Locate every uninfected red blood cell.
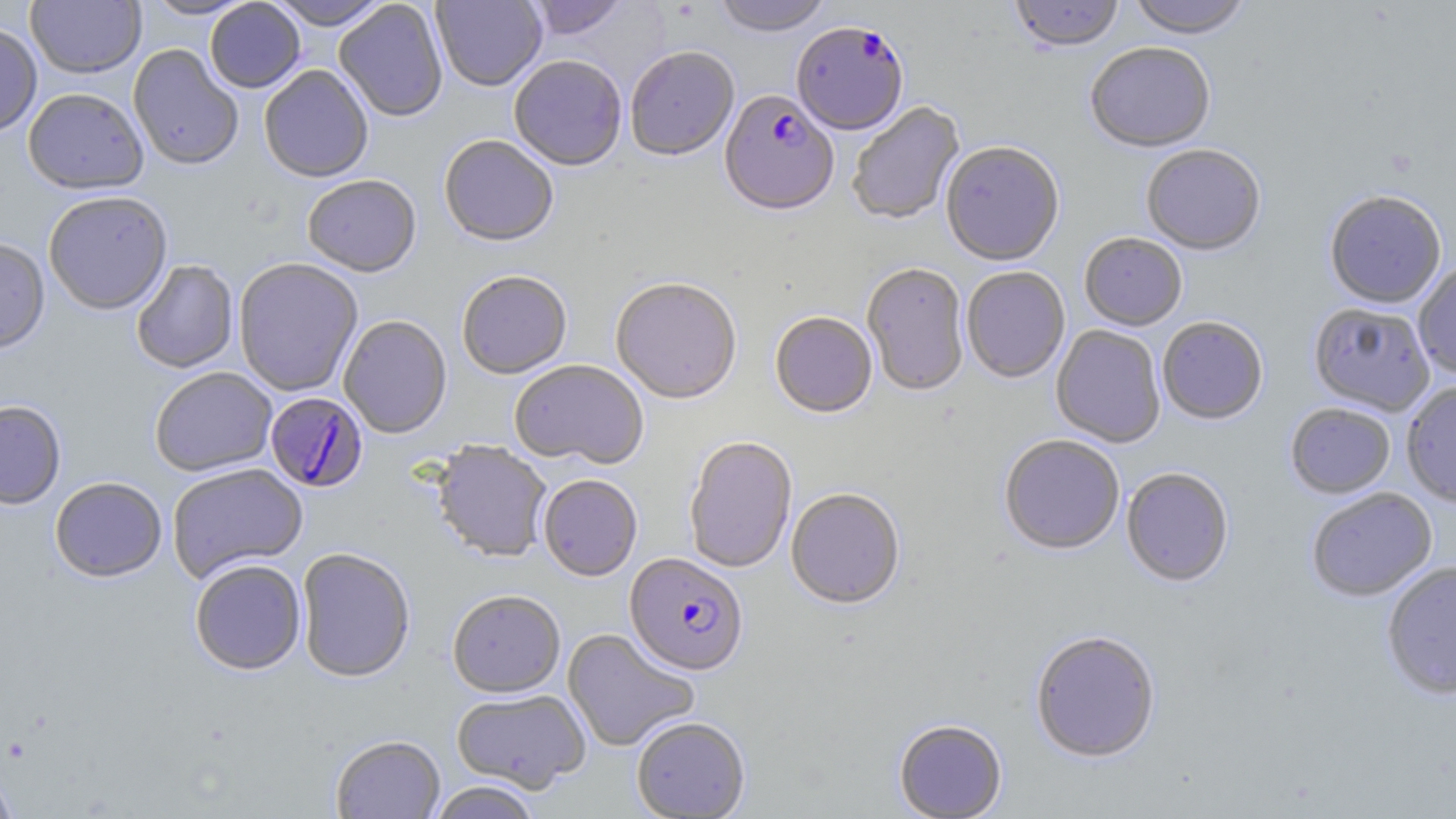
Approximate bounding boxes as (x1,y1)-(x2,y2) corner pairs in pixels.
Uninfected red blood cells: (142,0)-(257,20), (267,0)-(391,31), (431,0)-(547,93), (525,0)-(629,41), (712,0)-(833,39), (1010,0)-(1124,55), (1126,0)-(1253,42), (26,1)-(146,79), (205,1)-(306,94), (334,1)-(448,123), (0,22)-(42,136), (128,45)-(244,171), (1085,45)-(1216,156), (625,49)-(739,164), (509,57)-(627,173), (259,66)-(374,185), (23,88)-(148,196), (848,102)-(966,226), (438,136)-(558,249), (940,143)-(1065,268), (1142,146)-(1266,258), (302,177)-(421,279), (43,193)-(173,316), (1324,193)-(1446,310), (1079,235)-(1188,332), (0,238)-(50,355), (233,259)-(363,397), (131,260)-(239,374), (862,264)-(970,398), (1413,264)-(1456,378), (961,268)-(1070,384), (457,272)-(572,380), (610,279)-(742,406), (1308,304)-(1434,417), (770,314)-(877,420), (338,316)-(452,439), (1157,318)-(1268,426), (1051,325)-(1166,448), (509,360)-(648,470), (149,368)-(278,478), (1401,382)-(1456,508), (0,401)-(66,510), (1285,404)-(1395,500), (999,436)-(1124,557), (684,438)-(797,574), (431,443)-(552,564), (168,463)-(308,584), (1121,469)-(1234,589), (538,475)-(642,582), (50,477)-(167,584), (786,489)-(905,611), (1307,489)-(1437,602), (297,549)-(415,684), (190,561)-(306,676), (1382,563)-(1456,702), (447,591)-(565,700), (562,628)-(699,752), (1030,632)-(1161,765), (451,689)-(590,794), (631,718)-(750,818), (893,720)-(1007,818), (331,736)-(445,819), (0,766)-(18,819), (427,782)-(542,819).

Plasmodium falciparum-infected red blood cell locations: (791,24)-(908,138), (719,92)-(839,220), (265,393)-(369,493), (624,554)-(749,678). Slide-level diagnosis: Plasmodium falciparum. 1000x magnification. Image is 1456×819 pixels. Optical microscopy. Single field of view. Thin blood smear. May-Grünwald-Giemsa-stained preparation.